Locate every white blood cell.
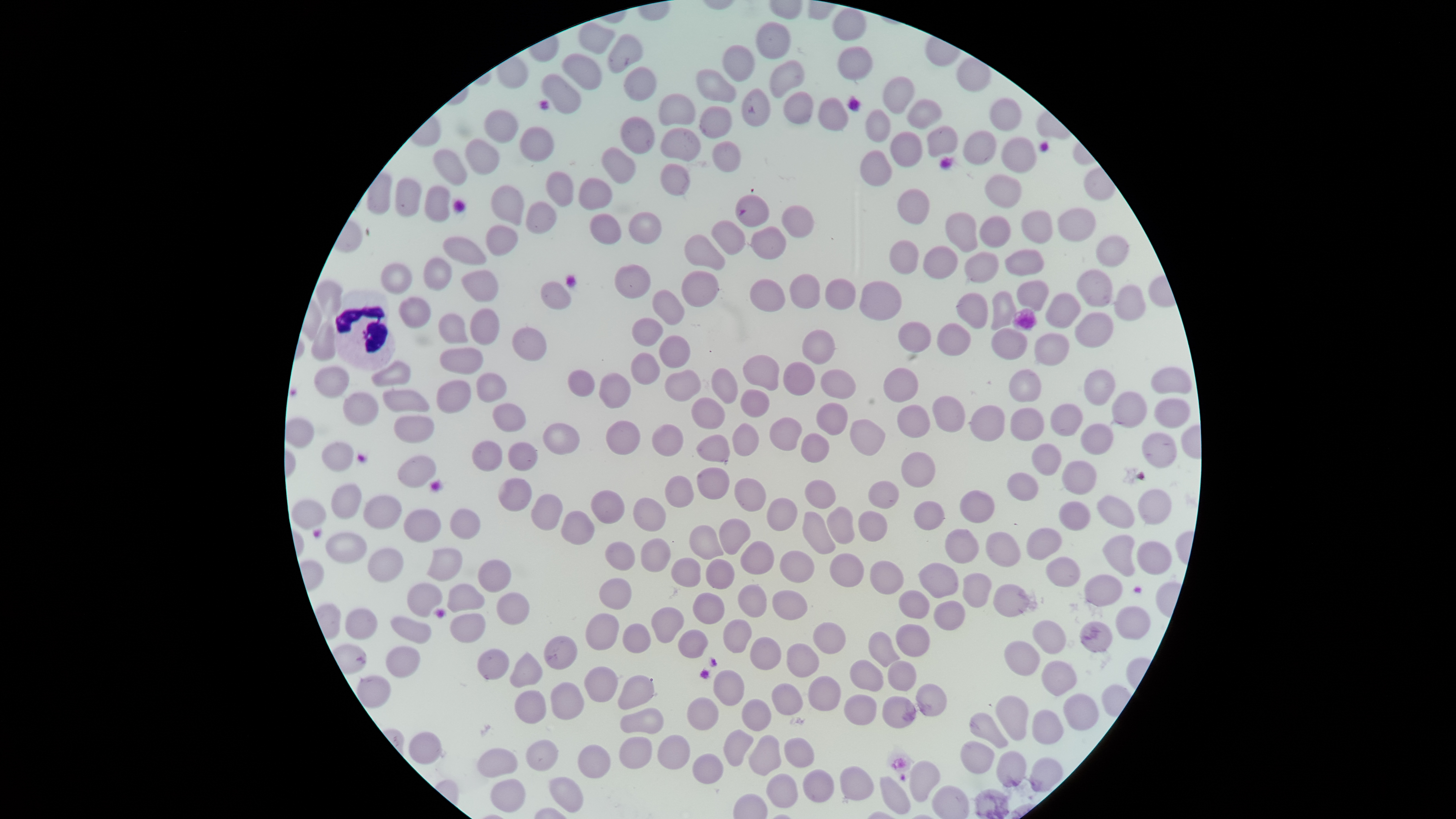

Approximate bounding boxes, in pixels from the top-left corner.
White blood cells: (left=334, top=289, right=396, bottom=371).

field of view = single
capture = smartphone photograph through the microscope eyepiece
image size = 1456×819 pixels
visible region = circular
presence = no malaria parasites identified
preparation = thin blood film
uninfected red blood cells = approximate bounding boxes, in pixels from the top-left corner: (left=832, top=9, right=867, bottom=41), (left=756, top=21, right=790, bottom=59), (left=578, top=23, right=615, bottom=55), (left=607, top=34, right=643, bottom=74), (left=722, top=44, right=755, bottom=82), (left=837, top=46, right=873, bottom=80), (left=561, top=54, right=602, bottom=90), (left=768, top=59, right=805, bottom=98), (left=623, top=66, right=657, bottom=102), (left=695, top=69, right=736, bottom=103), (left=541, top=74, right=581, bottom=114), (left=882, top=75, right=915, bottom=115), (left=741, top=88, right=770, bottom=127), (left=783, top=91, right=814, bottom=125), (left=657, top=93, right=695, bottom=126), (left=818, top=97, right=849, bottom=131), (left=989, top=97, right=1023, bottom=131), (left=906, top=98, right=942, bottom=130), (left=698, top=106, right=732, bottom=139), (left=484, top=109, right=519, bottom=144), (left=865, top=109, right=890, bottom=143), (left=620, top=116, right=655, bottom=155), (left=927, top=125, right=958, bottom=157), (left=520, top=127, right=555, bottom=162), (left=659, top=127, right=702, bottom=162), (left=962, top=130, right=997, bottom=166), (left=889, top=131, right=922, bottom=168), (left=1000, top=136, right=1037, bottom=173), (left=463, top=138, right=499, bottom=176), (left=711, top=141, right=741, bottom=173), (left=601, top=147, right=636, bottom=184), (left=433, top=149, right=468, bottom=186), (left=859, top=150, right=891, bottom=187), (left=660, top=163, right=691, bottom=196), (left=545, top=172, right=574, bottom=207), (left=984, top=174, right=1022, bottom=208), (left=394, top=178, right=422, bottom=217), (left=577, top=178, right=612, bottom=210), (left=490, top=185, right=525, bottom=226), (left=424, top=186, right=450, bottom=223), (left=897, top=188, right=930, bottom=225), (left=735, top=194, right=769, bottom=227), (left=525, top=201, right=557, bottom=235), (left=781, top=205, right=814, bottom=239), (left=1057, top=208, right=1097, bottom=242), (left=1021, top=211, right=1053, bottom=244), (left=628, top=212, right=661, bottom=245), (left=945, top=212, right=979, bottom=253), (left=589, top=213, right=622, bottom=245), (left=979, top=216, right=1011, bottom=248), (left=711, top=220, right=746, bottom=255), (left=486, top=225, right=517, bottom=256), (left=750, top=226, right=786, bottom=260), (left=684, top=234, right=726, bottom=270), (left=442, top=236, right=487, bottom=266), (left=1095, top=236, right=1129, bottom=267), (left=889, top=240, right=919, bottom=275), (left=922, top=246, right=958, bottom=278), (left=1004, top=249, right=1045, bottom=276), (left=963, top=252, right=999, bottom=283), (left=423, top=258, right=452, bottom=291), (left=380, top=264, right=413, bottom=295), (left=614, top=264, right=651, bottom=299), (left=460, top=270, right=499, bottom=302), (left=681, top=270, right=719, bottom=307), (left=1076, top=270, right=1112, bottom=308), (left=789, top=273, right=820, bottom=309), (left=825, top=278, right=856, bottom=310), (left=749, top=279, right=785, bottom=312), (left=315, top=280, right=342, bottom=317), (left=1017, top=280, right=1049, bottom=312), (left=540, top=281, right=572, bottom=311), (left=860, top=281, right=902, bottom=321), (left=1113, top=285, right=1146, bottom=320), (left=652, top=290, right=685, bottom=326), (left=990, top=291, right=1017, bottom=331), (left=956, top=292, right=988, bottom=330), (left=1045, top=293, right=1081, bottom=329), (left=398, top=296, right=431, bottom=329), (left=469, top=308, right=499, bottom=346), (left=437, top=313, right=468, bottom=345), (left=1074, top=313, right=1113, bottom=348), (left=631, top=318, right=663, bottom=347), (left=310, top=322, right=335, bottom=361), (left=898, top=322, right=932, bottom=353), (left=936, top=323, right=971, bottom=357), (left=511, top=327, right=547, bottom=362), (left=990, top=328, right=1028, bottom=360), (left=801, top=329, right=835, bottom=365), (left=1033, top=333, right=1070, bottom=366), (left=659, top=336, right=691, bottom=369), (left=439, top=348, right=483, bottom=375), (left=630, top=353, right=660, bottom=385), (left=742, top=355, right=779, bottom=392), (left=371, top=360, right=411, bottom=387), (left=783, top=361, right=816, bottom=396), (left=313, top=366, right=350, bottom=398), (left=1151, top=367, right=1191, bottom=394), (left=711, top=368, right=738, bottom=405), (left=883, top=368, right=919, bottom=403), (left=664, top=369, right=700, bottom=402), (left=819, top=369, right=856, bottom=399), (left=1008, top=369, right=1042, bottom=403), (left=1083, top=369, right=1115, bottom=406), (left=567, top=370, right=596, bottom=397), (left=598, top=372, right=631, bottom=409), (left=476, top=373, right=507, bottom=403), (left=436, top=380, right=470, bottom=413), (left=382, top=389, right=429, bottom=413), (left=740, top=389, right=770, bottom=417), (left=343, top=392, right=379, bottom=426), (left=1111, top=392, right=1147, bottom=429), (left=932, top=396, right=965, bottom=432), (left=691, top=398, right=726, bottom=429), (left=1153, top=398, right=1191, bottom=429), (left=816, top=402, right=848, bottom=436), (left=492, top=403, right=526, bottom=433), (left=1050, top=403, right=1082, bottom=437), (left=897, top=404, right=931, bottom=438), (left=969, top=404, right=1004, bottom=442), (left=1010, top=407, right=1045, bottom=442), (left=393, top=415, right=435, bottom=444), (left=768, top=417, right=802, bottom=451), (left=850, top=419, right=885, bottom=456), (left=605, top=420, right=640, bottom=456), (left=542, top=423, right=581, bottom=455), (left=732, top=423, right=759, bottom=457), (left=1080, top=423, right=1113, bottom=455), (left=652, top=424, right=684, bottom=457), (left=1142, top=432, right=1177, bottom=468), (left=800, top=433, right=829, bottom=463), (left=695, top=434, right=730, bottom=463), (left=472, top=440, right=503, bottom=472), (left=321, top=442, right=354, bottom=472), (left=507, top=442, right=538, bottom=472), (left=1031, top=444, right=1062, bottom=476), (left=900, top=452, right=936, bottom=488), (left=396, top=454, right=436, bottom=488), (left=1061, top=461, right=1096, bottom=496), (left=696, top=467, right=729, bottom=500), (left=1006, top=473, right=1038, bottom=501), (left=663, top=476, right=694, bottom=508), (left=497, top=477, right=531, bottom=512), (left=734, top=478, right=766, bottom=512), (left=804, top=479, right=836, bottom=510), (left=868, top=481, right=899, bottom=509), (left=331, top=482, right=362, bottom=519), (left=1138, top=489, right=1172, bottom=525), (left=589, top=490, right=626, bottom=525), (left=959, top=490, right=995, bottom=523), (left=531, top=494, right=562, bottom=531), (left=363, top=495, right=402, bottom=529), (left=1096, top=495, right=1134, bottom=529), (left=632, top=497, right=666, bottom=532), (left=766, top=497, right=798, bottom=532), (left=291, top=499, right=326, bottom=530), (left=913, top=501, right=944, bottom=530), (left=1058, top=501, right=1091, bottom=531), (left=826, top=506, right=855, bottom=545), (left=449, top=508, right=480, bottom=540), (left=403, top=509, right=441, bottom=543), (left=560, top=511, right=595, bottom=545), (left=858, top=511, right=887, bottom=542), (left=802, top=512, right=837, bottom=555), (left=719, top=518, right=750, bottom=555), (left=688, top=525, right=724, bottom=559), (left=1026, top=528, right=1062, bottom=560), (left=945, top=529, right=979, bottom=564), (left=985, top=531, right=1022, bottom=567), (left=325, top=532, right=368, bottom=563), (left=1102, top=534, right=1136, bottom=577), (left=640, top=538, right=671, bottom=572), (left=739, top=540, right=774, bottom=574), (left=604, top=541, right=636, bottom=571), (left=1136, top=541, right=1173, bottom=574), (left=367, top=547, right=404, bottom=583), (left=427, top=548, right=463, bottom=582), (left=779, top=550, right=814, bottom=583), (left=829, top=553, right=865, bottom=587), (left=1046, top=556, right=1080, bottom=587), (left=670, top=557, right=701, bottom=588), (left=705, top=558, right=734, bottom=589), (left=477, top=560, right=512, bottom=593), (left=869, top=560, right=904, bottom=594), (left=919, top=563, right=959, bottom=599), (left=962, top=572, right=992, bottom=608), (left=1084, top=573, right=1123, bottom=607), (left=598, top=578, right=632, bottom=610), (left=992, top=582, right=1028, bottom=618), (left=407, top=583, right=443, bottom=617), (left=446, top=583, right=486, bottom=613), (left=737, top=584, right=767, bottom=618), (left=771, top=590, right=808, bottom=620), (left=898, top=590, right=930, bottom=619), (left=496, top=592, right=529, bottom=625), (left=692, top=593, right=724, bottom=624), (left=934, top=601, right=965, bottom=631), (left=1115, top=606, right=1151, bottom=640), (left=650, top=607, right=684, bottom=644), (left=344, top=608, right=378, bottom=640), (left=449, top=613, right=486, bottom=644), (left=585, top=613, right=619, bottom=651), (left=390, top=615, right=432, bottom=644), (left=722, top=618, right=752, bottom=653), (left=1032, top=619, right=1065, bottom=654), (left=1079, top=621, right=1113, bottom=653), (left=812, top=622, right=847, bottom=655), (left=622, top=623, right=651, bottom=654), (left=895, top=623, right=931, bottom=657), (left=677, top=629, right=708, bottom=659), (left=867, top=631, right=898, bottom=667), (left=543, top=635, right=578, bottom=670), (left=749, top=636, right=781, bottom=670), (left=1003, top=641, right=1040, bottom=675), (left=786, top=643, right=819, bottom=678), (left=385, top=645, right=420, bottom=678), (left=477, top=648, right=509, bottom=679), (left=509, top=651, right=543, bottom=688), (left=848, top=660, right=884, bottom=692), (left=886, top=660, right=917, bottom=691), (left=1041, top=660, right=1076, bottom=696), (left=584, top=666, right=618, bottom=703), (left=712, top=669, right=744, bottom=706), (left=356, top=675, right=390, bottom=709), (left=618, top=675, right=655, bottom=710), (left=806, top=675, right=840, bottom=712), (left=550, top=682, right=584, bottom=720), (left=771, top=683, right=804, bottom=716), (left=916, top=683, right=947, bottom=717), (left=514, top=690, right=546, bottom=724), (left=1063, top=693, right=1099, bottom=730), (left=844, top=694, right=877, bottom=726), (left=882, top=695, right=916, bottom=728), (left=995, top=695, right=1028, bottom=741), (left=686, top=697, right=719, bottom=731), (left=741, top=698, right=771, bottom=732), (left=619, top=707, right=664, bottom=735), (left=1031, top=710, right=1063, bottom=744), (left=969, top=712, right=1008, bottom=749), (left=723, top=729, right=753, bottom=766), (left=408, top=731, right=441, bottom=765), (left=657, top=734, right=690, bottom=770), (left=748, top=734, right=782, bottom=775), (left=619, top=737, right=653, bottom=769), (left=783, top=737, right=815, bottom=768), (left=524, top=738, right=558, bottom=772), (left=960, top=741, right=994, bottom=775), (left=578, top=745, right=611, bottom=778), (left=476, top=748, right=518, bottom=778), (left=995, top=751, right=1027, bottom=787), (left=692, top=754, right=724, bottom=784), (left=909, top=760, right=940, bottom=802), (left=839, top=766, right=874, bottom=801), (left=801, top=769, right=835, bottom=803), (left=766, top=773, right=798, bottom=808), (left=880, top=776, right=910, bottom=814), (left=548, top=777, right=583, bottom=813), (left=490, top=779, right=525, bottom=813)
stain = Giemsa